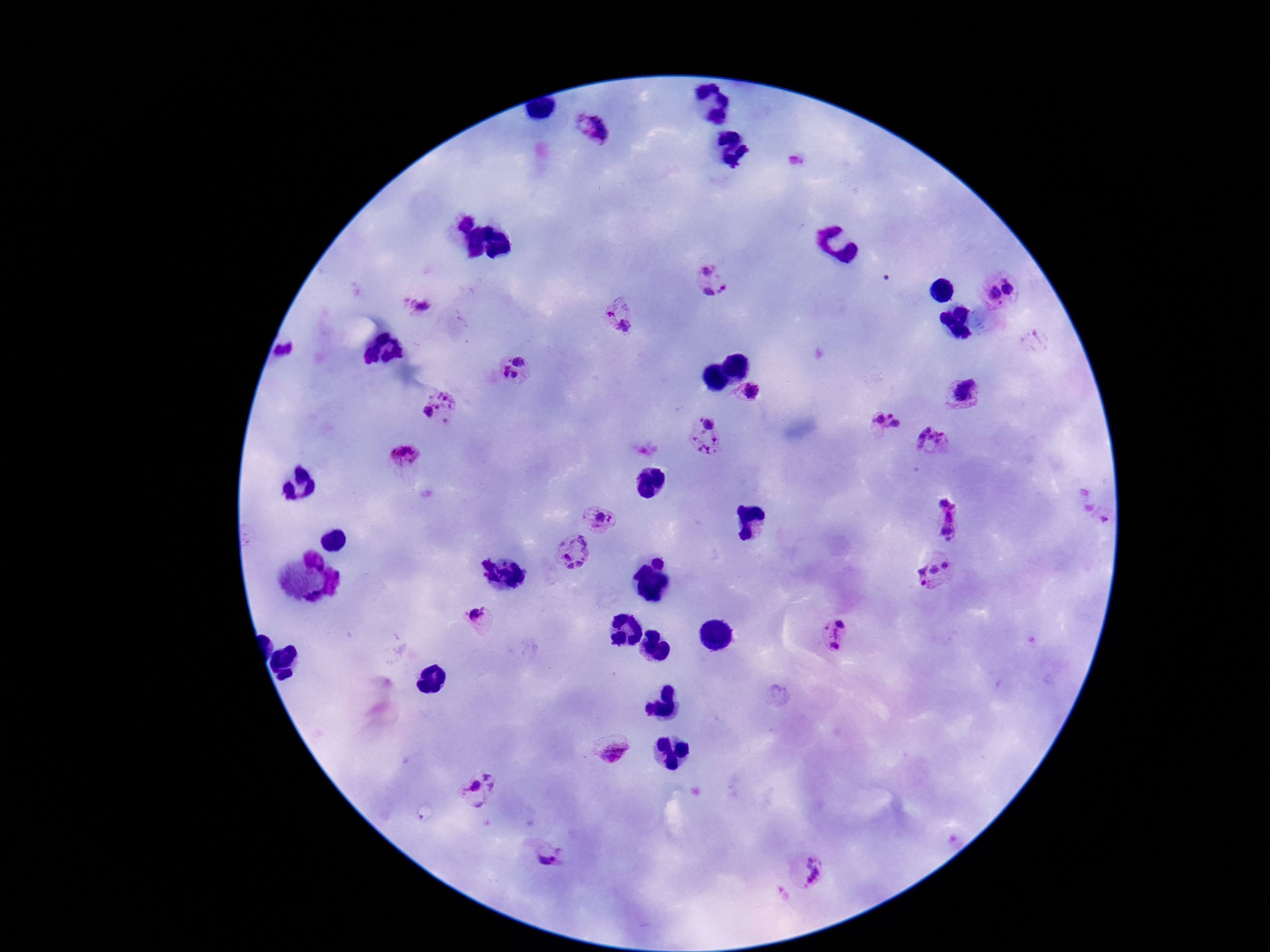
image size = 1270×952 pixels
field of view = one from this slide
magnification = 100x
Plasmodium parasite locations = approximate object centers, in pixels from the top-left corner: (x=593, y=129), (x=461, y=219), (x=708, y=281), (x=1000, y=290), (x=419, y=304), (x=621, y=315), (x=514, y=371), (x=754, y=394), (x=964, y=396), (x=441, y=407), (x=886, y=423), (x=705, y=438), (x=935, y=441), (x=403, y=455), (x=1095, y=516), (x=601, y=519), (x=947, y=521), (x=573, y=554), (x=935, y=571), (x=480, y=615), (x=833, y=635), (x=612, y=751), (x=481, y=792), (x=547, y=854), (x=808, y=872)
capture = smartphone camera through the microscope eyepiece
stain = Giemsa
preparation = thick blood film
patient malaria status = positive